Identify the parasite.
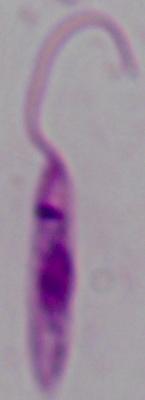
This is Leishmania.

Photomicrograph. Captured at 1000x magnification.